Assess this cell for malaria.
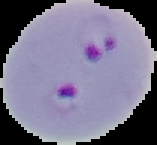
It is parasitized.

Summary:
  - Preparation: thin blood film
  - Image size: 157×145 pixels
  - Image type: segmented cell region with the area outside set to black